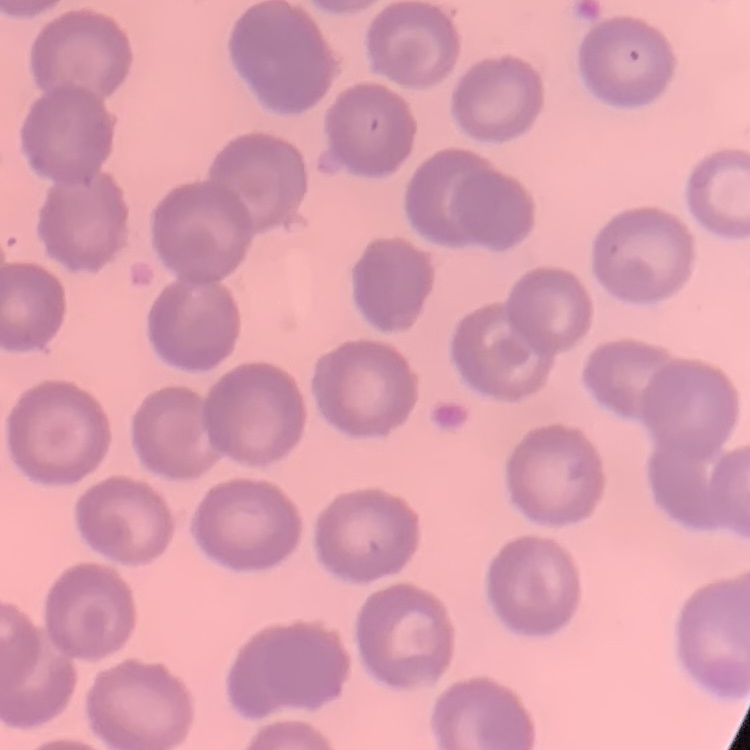

Summary:
  - Erythrocyte morphology: no rouleaux formation
  - Image type: one tile cut from a larger photomicrograph
  - Preparation: thin peripheral smear
  - Stain: Field's or Giemsa